Report the malaria status of this cell.
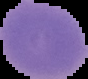
It is uninfected.

{
  "preparation": "thin blood film",
  "image_size": "88×79 pixels",
  "image_type": "segmented cell region on a black background"
}